Classify this cell by malaria status.
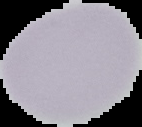
It is uninfected.

image size = 142×127 pixels
image type = segmented cell region with the area outside set to black
preparation = thin blood film